Identify the parasite.
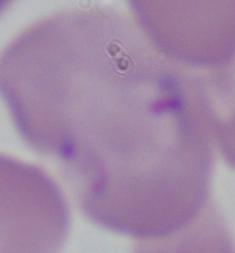
Babesia.

{
  "magnification": "1000x",
  "modality": "micrograph"
}